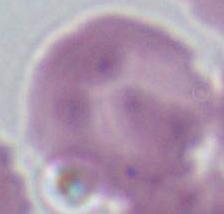

Summary:
  - Modality: micrograph
  - Magnification: 1000x
  - Identification: red blood cell